Identify the cell.
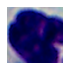

This is a leukocyte.

{
  "magnification": "1000x",
  "modality": "micrograph"
}